Report the malaria status of this cell.
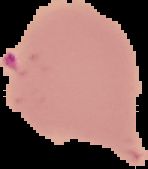

It is parasitized.

From a thin blood film. Segmented cell region on a black background. Image is 148×169 pixels.